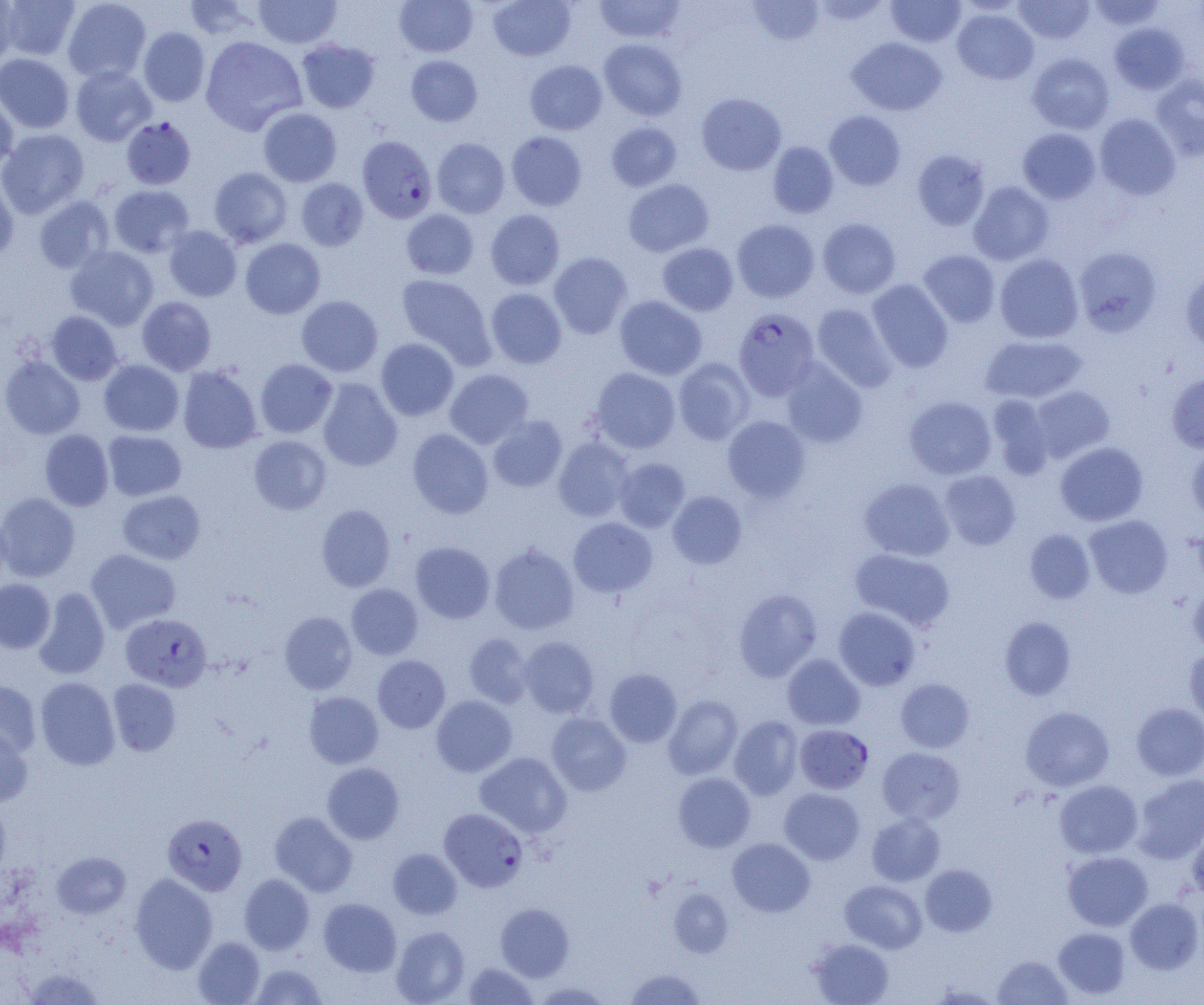

Approximate bounding boxes as (x1, y1, x2, y2) in pixels. Plasmodium falciparum-infected red blood cell locations: (121, 117, 196, 190), (360, 137, 439, 224), (733, 308, 820, 400), (121, 613, 212, 691), (795, 724, 874, 794), (440, 807, 528, 892), (162, 813, 247, 895). Uninfected red blood cell locations: (0, 0, 22, 67), (2, 0, 81, 61), (62, 0, 151, 83), (254, 0, 343, 48), (394, 0, 478, 57), (487, 0, 575, 61), (594, 0, 686, 43), (747, 0, 824, 46), (1013, 0, 1095, 44), (1087, 0, 1167, 31), (182, 1, 262, 41), (811, 1, 891, 25), (885, 1, 966, 47), (952, 8, 1039, 85), (1109, 22, 1189, 94), (138, 27, 210, 106), (200, 36, 307, 135), (847, 36, 946, 115), (296, 39, 380, 113), (599, 39, 687, 121), (0, 53, 75, 133), (1027, 53, 1114, 134), (406, 55, 482, 127), (525, 60, 607, 135), (71, 66, 156, 146), (1151, 74, 1204, 160), (0, 91, 18, 173), (697, 92, 786, 175), (258, 108, 342, 187), (824, 110, 906, 190), (1094, 113, 1181, 200), (606, 121, 682, 191), (1018, 128, 1101, 204), (0, 129, 89, 218), (506, 131, 587, 210), (432, 138, 510, 218), (768, 142, 838, 218), (912, 149, 991, 231), (209, 167, 293, 248), (0, 175, 19, 264), (295, 178, 368, 251), (623, 179, 714, 257), (968, 181, 1054, 265), (108, 185, 194, 257), (33, 196, 115, 274), (401, 209, 479, 279), (485, 209, 565, 290), (817, 218, 901, 299), (732, 219, 819, 303), (163, 225, 242, 301), (240, 238, 325, 319), (657, 242, 739, 316), (65, 246, 158, 330), (1073, 246, 1162, 337), (918, 250, 1001, 327), (548, 252, 632, 339), (994, 254, 1083, 343), (1180, 268, 1204, 355), (396, 274, 495, 367), (867, 279, 953, 372), (485, 288, 567, 369), (296, 295, 382, 376), (614, 295, 707, 380), (137, 296, 216, 375), (811, 303, 897, 391), (46, 311, 122, 385), (981, 335, 1087, 404), (376, 338, 459, 421), (0, 356, 85, 439), (673, 358, 755, 444), (780, 358, 867, 448), (255, 359, 337, 438), (99, 360, 184, 436), (177, 366, 262, 453), (591, 367, 680, 453), (445, 369, 533, 449), (1167, 373, 1204, 453), (317, 378, 402, 471), (1030, 385, 1115, 462), (988, 395, 1054, 479), (904, 396, 996, 480), (488, 416, 566, 493), (722, 416, 811, 502), (407, 428, 493, 518), (39, 429, 114, 511), (102, 430, 186, 501), (249, 435, 331, 514), (553, 437, 634, 522), (1055, 441, 1148, 526), (1186, 442, 1204, 524), (614, 457, 690, 532), (939, 470, 1021, 550), (860, 478, 955, 561), (117, 490, 206, 564), (668, 491, 747, 568), (0, 492, 80, 582), (317, 504, 395, 591), (0, 512, 11, 591), (1084, 515, 1173, 598), (568, 517, 657, 598), (1024, 528, 1096, 603), (410, 541, 495, 624), (489, 544, 579, 634), (850, 548, 955, 631), (85, 549, 181, 633), (0, 578, 55, 654), (1188, 579, 1204, 656), (346, 584, 424, 659), (33, 588, 110, 679), (733, 588, 822, 682), (833, 607, 920, 690), (279, 611, 357, 694), (999, 617, 1076, 700), (463, 633, 533, 708), (518, 636, 599, 718), (1185, 648, 1204, 729), (782, 654, 865, 730), (373, 655, 450, 733), (605, 668, 682, 747), (35, 677, 120, 770), (896, 678, 975, 752), (107, 679, 181, 756), (0, 680, 42, 759), (303, 692, 383, 769), (431, 695, 517, 777), (664, 695, 743, 779), (1131, 702, 1204, 781), (1020, 706, 1114, 791), (546, 712, 631, 795), (729, 716, 803, 799), (0, 722, 33, 808), (877, 747, 965, 824), (475, 752, 572, 837), (322, 763, 404, 844), (673, 772, 755, 852), (1132, 774, 1204, 863), (1054, 780, 1142, 858), (779, 788, 865, 864), (0, 799, 11, 886), (270, 811, 357, 896), (866, 813, 944, 886), (1186, 822, 1204, 902), (727, 837, 815, 916), (388, 848, 462, 919), (52, 851, 131, 918), (1063, 851, 1153, 930), (920, 864, 997, 936), (129, 873, 218, 973), (239, 874, 314, 954), (840, 880, 927, 953), (669, 888, 733, 957), (318, 898, 401, 976), (1125, 898, 1203, 974), (495, 903, 574, 981), (391, 926, 470, 1004), (1054, 927, 1130, 999), (193, 937, 265, 1004), (808, 938, 894, 1005), (993, 955, 1072, 1004), (463, 962, 538, 1004), (250, 963, 327, 1005), (22, 968, 106, 1004), (624, 968, 707, 1005), (530, 981, 614, 1004). Slide-level diagnosis: Plasmodium falciparum. Light microscopy. Captured at 1000x magnification. Thin blood smear. Image is 1204×1005 pixels. One field of a larger specimen.